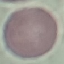

Summary:
  - Result: negative for malaria parasites
  - Preparation: thin smear
  - Capture: smartphone through the microscope eyepiece
  - Stain: Giemsa
  - Image type: automatically extracted cell patch, resized to 64 × 64 pixels